State which parasite is depicted.
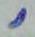

Toxoplasma gondii.

modality = micrograph
magnification = 1000x